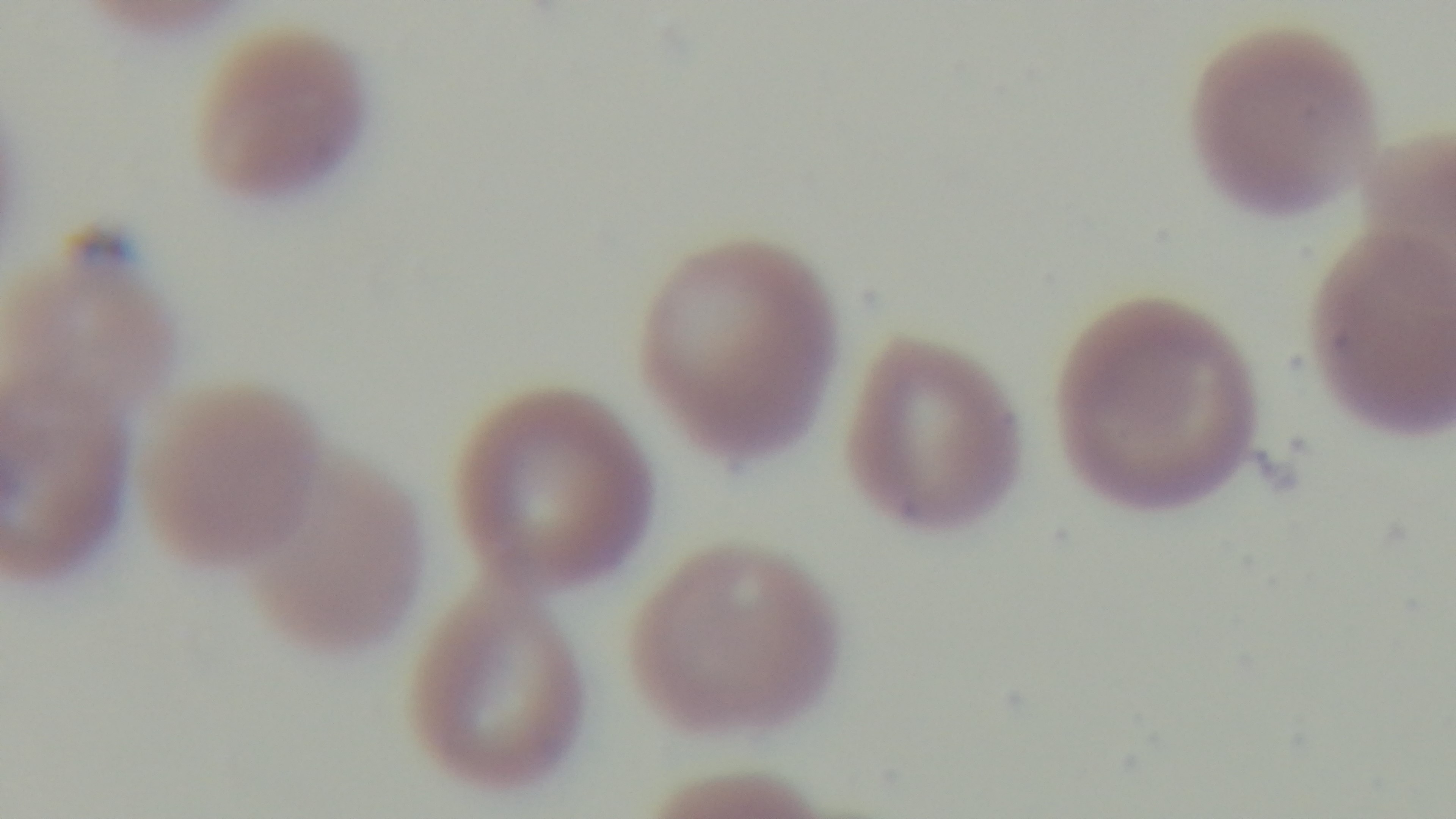
Single field of view. Captured with a mounted 4K digital camera. Malaria status: positive. Giemsa-stained. Preparation: thin blood film. Photomicrograph. 100x oil-immersion objective.